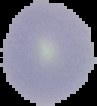
image size = 97×106 pixels
image type = segmented cell region with the area outside set to black
malaria status = uninfected
preparation = thin blood smear